Assess the morphology of the erythrocytes.
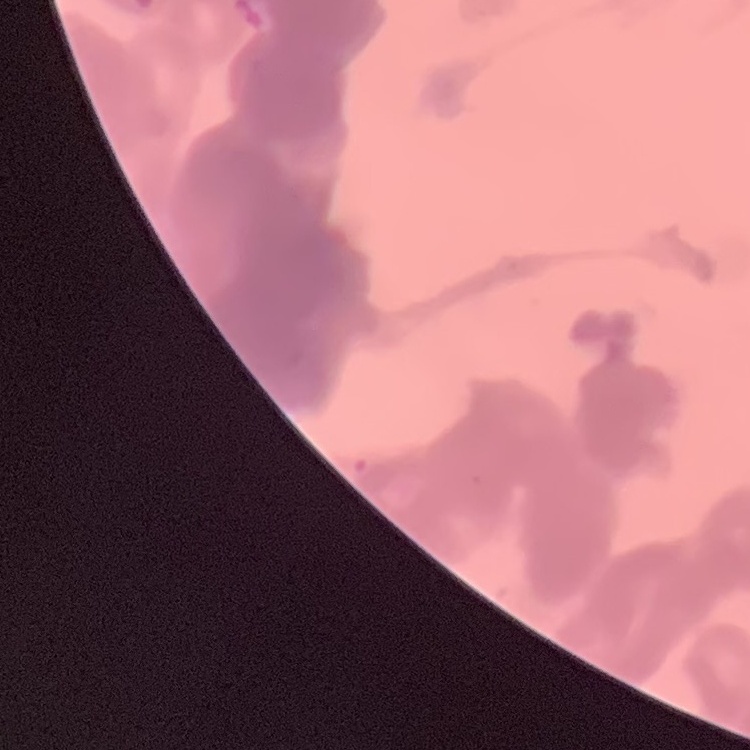
They show rouleaux formation.

preparation = thin blood film
image type = one tile cut from a larger photomicrograph
stain = Field's or Giemsa